Assess this cell for malaria.
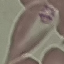
It is parasitized.

{
  "preparation": "thin blood smear",
  "stain": "Giemsa",
  "image_type": "cell patch, automatically extracted from a larger field of view and resized to 64 × 64 pixels",
  "capture": "smartphone through the microscope eyepiece"
}